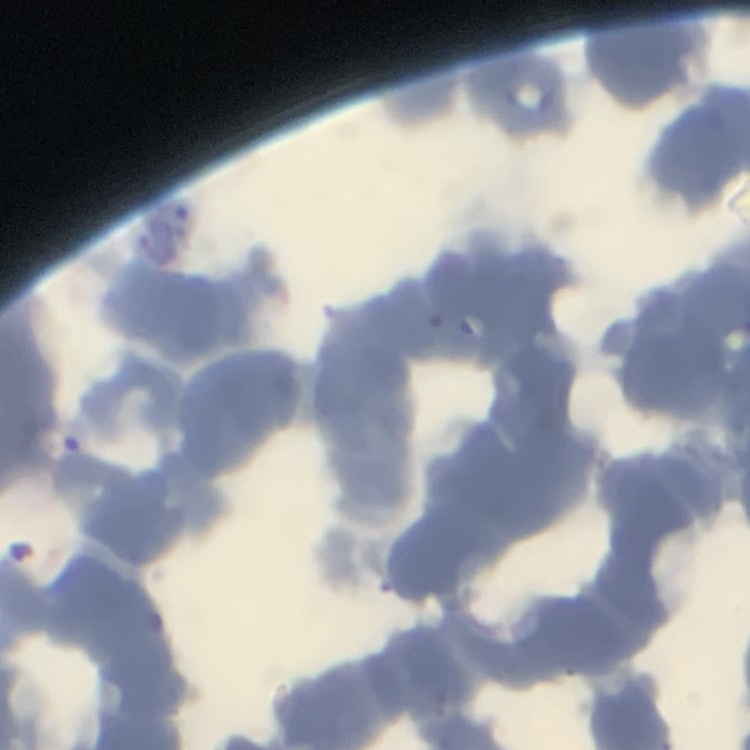

Summary:
  - Red blood cell morphology: rouleaux formation
  - Preparation: thin peripheral smear
  - Image type: square crop of a larger photomicrograph
  - Stain: Field's or Giemsa